Assess this cell for malaria.
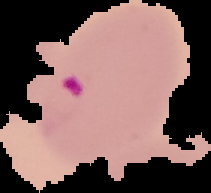

Parasitized.

preparation = thin blood smear
image type = segmented cell region on a black background
image size = 211×193 pixels